Point out each malaria parasite.
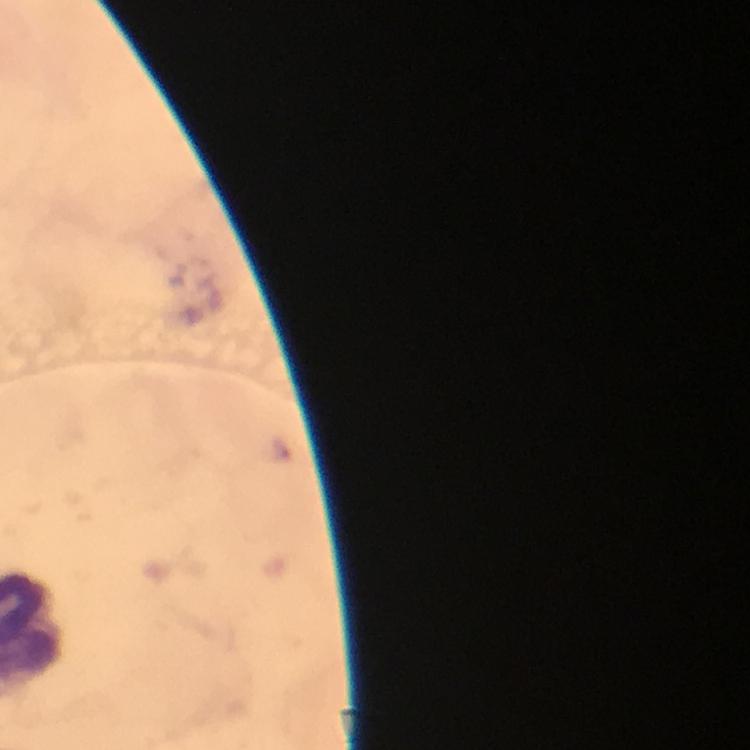

Approximate centers as {x, y} in pixels.
Malaria parasites: {280, 450}.

magnification: 100x
stain: Giemsa
immersion_oil: applied
image_size: 750×750 pixels
cropped_from: a single field of view
context: from a diagnostic examination for malaria
capture: smartphone mounted on the microscope
preparation: thick blood film